Locate every blood parasite and identify its species.
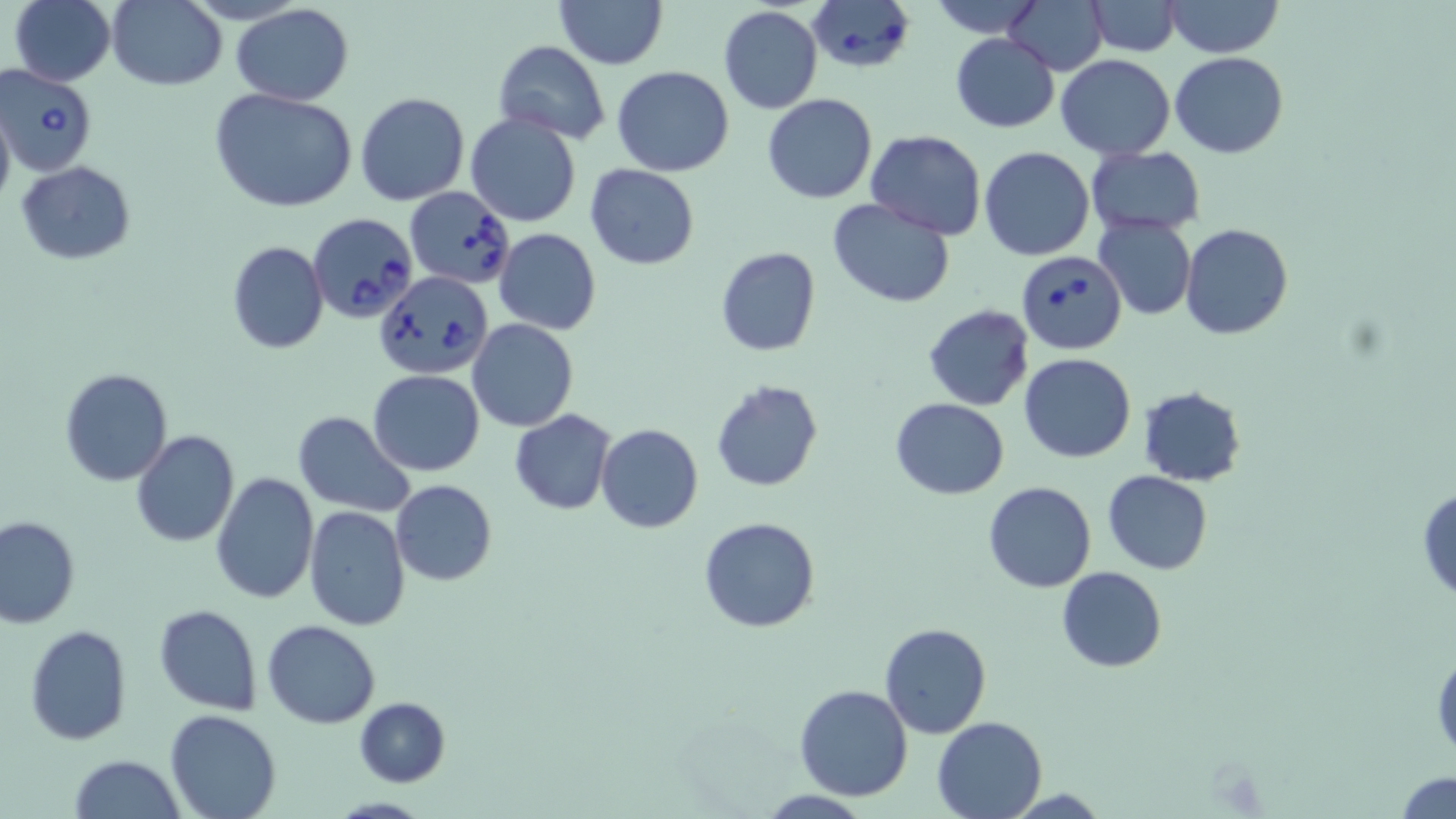
Approximate bounding boxes as (x1, y1, x2, y2) in pixels.
Babesia divergens-infected red blood cells: (807, 0, 915, 72), (1, 64, 98, 175), (405, 186, 515, 291), (305, 212, 423, 324), (1017, 251, 1127, 354), (375, 271, 491, 380).
No Plasmodium falciparum, Plasmodium ovale, Plasmodium malariae, Plasmodium vivax, or Trypanosoma brucei observed.

Summary:
  - Uninfected red blood cell locations: (10, 0, 117, 87), (928, 0, 1044, 37), (1004, 0, 1108, 74), (1166, 0, 1283, 57), (106, 1, 226, 90), (554, 1, 668, 69), (1087, 1, 1179, 56), (231, 4, 355, 107), (718, 6, 822, 113), (950, 32, 1060, 132), (494, 40, 610, 146), (1172, 52, 1289, 158), (1055, 55, 1177, 160), (612, 65, 735, 176), (210, 88, 358, 213), (355, 92, 468, 205), (762, 94, 879, 204), (0, 95, 16, 220), (464, 114, 583, 227), (866, 130, 985, 240), (1085, 146, 1205, 235), (979, 147, 1096, 261), (15, 161, 136, 265), (583, 163, 701, 270), (828, 198, 956, 307), (1093, 216, 1196, 321), (1179, 223, 1293, 340), (493, 228, 601, 335), (227, 242, 330, 354), (716, 247, 821, 358), (923, 305, 1034, 410), (466, 319, 579, 433), (1018, 353, 1137, 463), (59, 368, 172, 485), (367, 370, 486, 476), (711, 380, 824, 493), (1138, 385, 1245, 487), (889, 396, 1010, 500), (509, 409, 617, 515), (294, 412, 416, 516), (596, 423, 703, 533), (132, 430, 239, 547), (1103, 471, 1213, 575), (210, 473, 318, 607), (390, 480, 497, 586), (983, 481, 1097, 594), (1417, 485, 1456, 604), (304, 506, 410, 630), (0, 514, 81, 628), (698, 517, 821, 634), (1056, 566, 1168, 673), (154, 605, 261, 714), (262, 619, 380, 728), (879, 622, 991, 738), (24, 624, 131, 746), (1432, 641, 1456, 767), (794, 684, 915, 801), (354, 697, 450, 787), (165, 710, 281, 819), (932, 715, 1048, 819), (69, 754, 186, 819), (1395, 771, 1456, 819)
  - Slide-level diagnosis: Babesia divergens
  - Preparation: thin blood smear
  - Stain: May-Grünwald-Giemsa
  - Modality: light microscopy
  - Magnification: 1000x
  - Field of view: single
  - Image size: 1456×819 pixels